Classify this cell by malaria status.
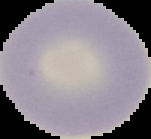

It is uninfected.

Summary:
  - Preparation: thin blood film
  - Image type: segmented cell region on a black background
  - Image size: 151×139 pixels